Give the position of every leukocyte visible.
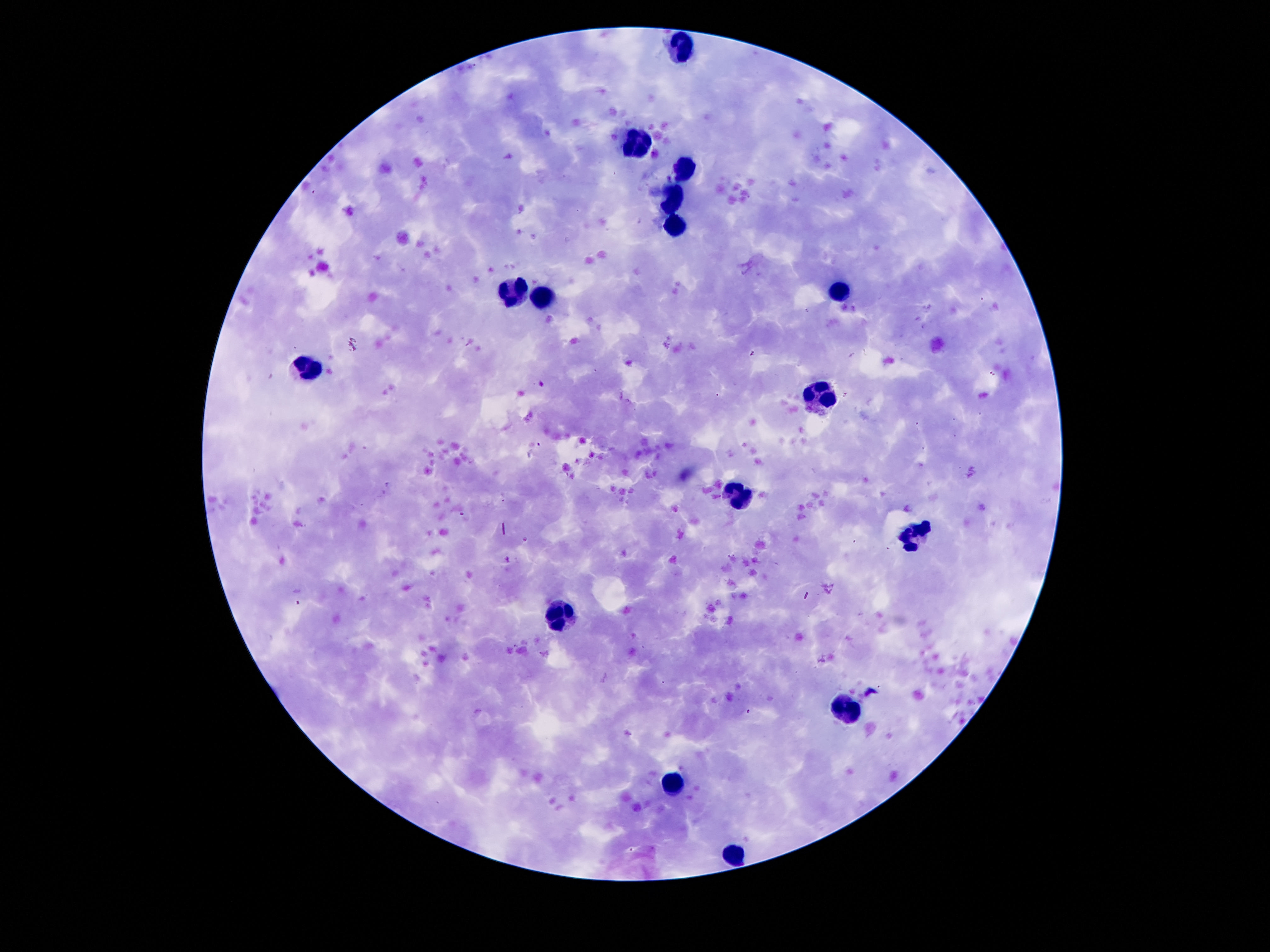

Approximate centers as {x, y} in pixels.
Leukocytes: {682, 46}, {637, 139}, {682, 169}, {673, 198}, {675, 225}, {839, 291}, {514, 294}, {543, 300}, {305, 366}, {823, 393}, {737, 496}, {918, 534}, {559, 616}, {843, 709}, {673, 782}, {734, 854}.

Thick peripheral-blood smear. Single field of view. 100x magnification. Patient malaria status: not infected. Smartphone photograph taken through the microscope eyepiece. Giemsa stain. Image is 1270×952 pixels.